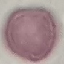
Summary:
  - Result: no malaria parasites seen
  - Image type: automatically extracted cell patch, resized to 64 × 64 pixels
  - Capture: smartphone through the microscope eyepiece
  - Preparation: thin blood smear
  - Stain: Giemsa